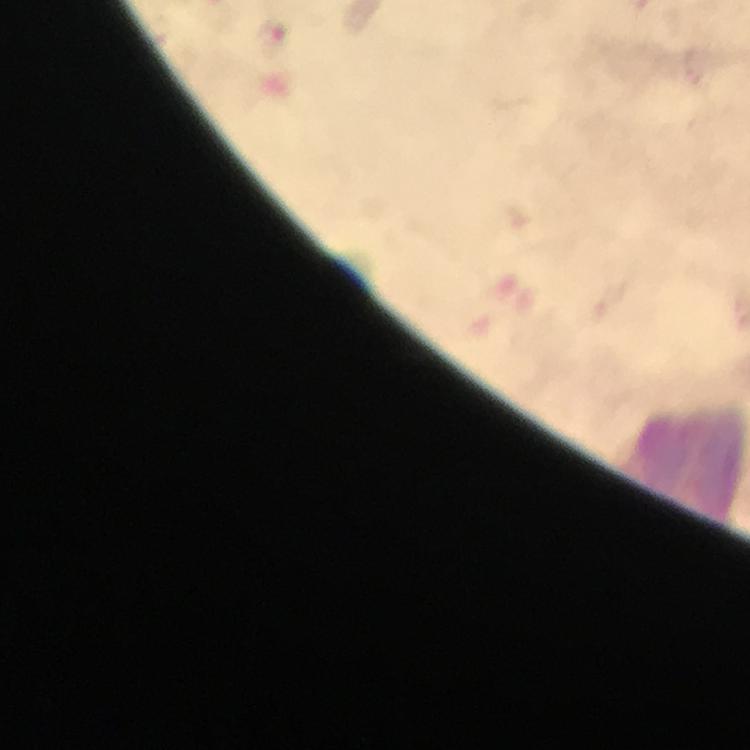 Approximate centers as (x, y) in pixels. Malaria parasite locations: (273, 39). Leukocyte locations: (687, 464). Photographed with a smartphone mounted on the microscope. Image is 750×750 pixels. Giemsa-stained preparation. Immersion oil applied. At 100x magnification. From a malaria diagnostic workup. A crop from one field of view. Thick smear.